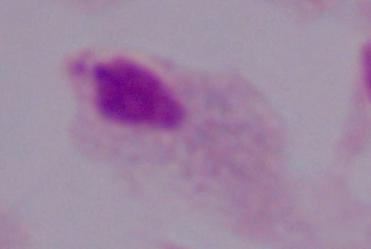

modality: photomicrograph
magnification: 1000x
identification: trichomonad